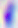

Summary:
  - Magnification: 400x
  - Identification: Toxoplasma gondii
  - Modality: photomicrograph